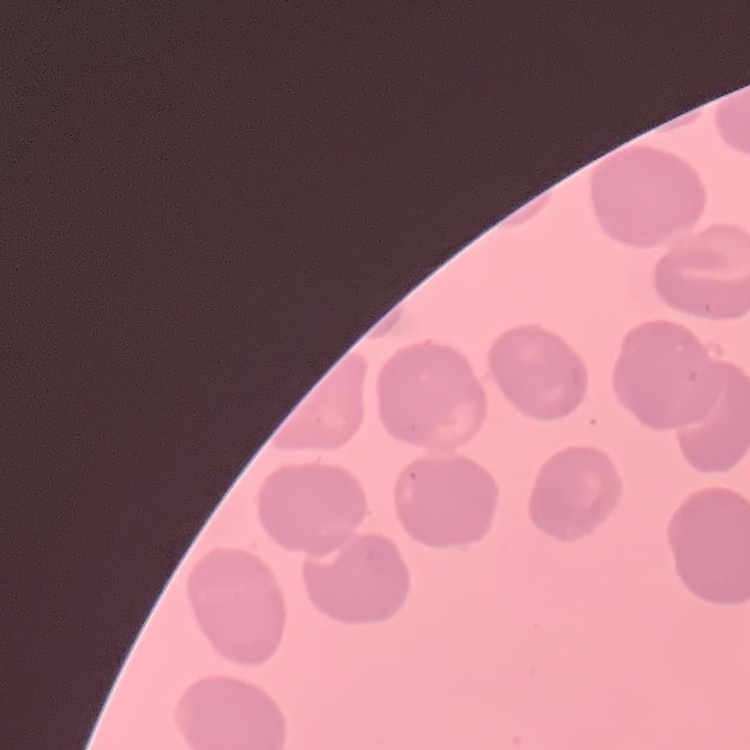

Summary:
  - Red blood cell morphology: no rouleaux formation
  - Preparation: thin blood smear
  - Image type: one tile cut from a larger photomicrograph
  - Stain: Field's or Giemsa